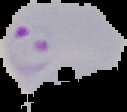

malaria status = parasitized
image type = segmented cell region on a black background
image size = 127×112 pixels
preparation = thin blood smear